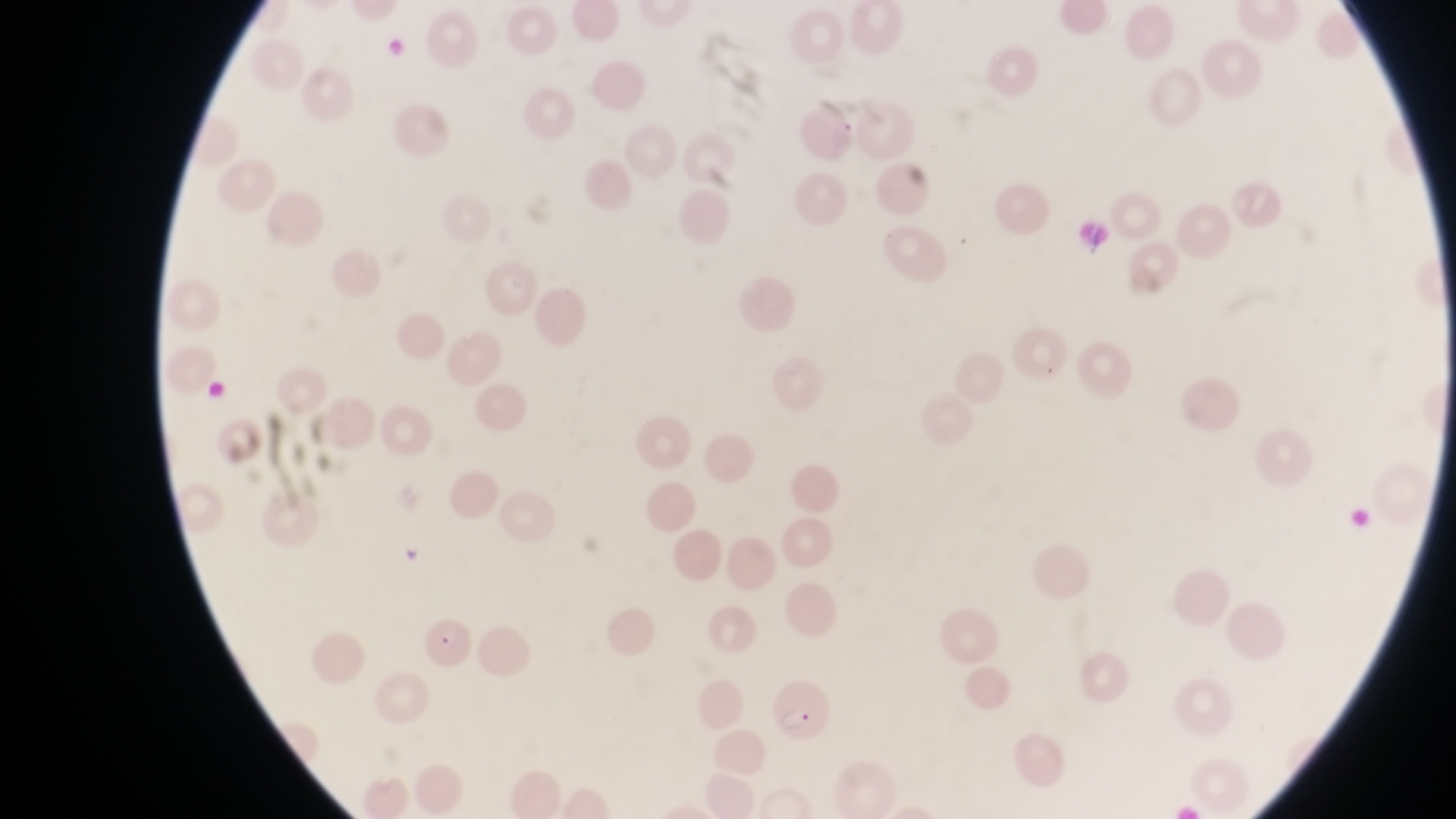
capture: smartphone photograph through the eyepiece of an Olympus CX-23 microscope
field_of_view: single
parasitised_red_blood_cell_locations: 'approximate bounding boxes as {left, top, right, bottom} in pixels: {419, 617, 477, 667}, {769, 680, 836, 744}'
preparation: thin blood smear
magnification: 1000x
image_size: 1456×819 pixels
country: Uganda